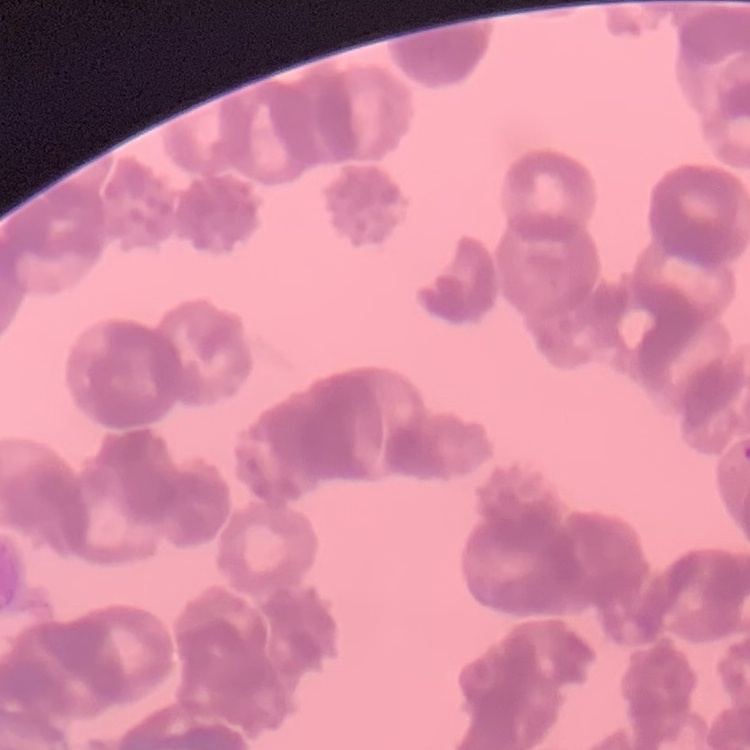

Summary:
  - Erythrocyte morphology: rouleaux formation
  - Stain: Field's or Giemsa
  - Preparation: thin peripheral smear
  - Image type: one tile cut from a larger photomicrograph